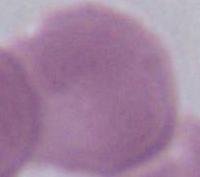
{
  "identification": "red blood cell",
  "magnification": "1000x",
  "modality": "photomicrograph"
}